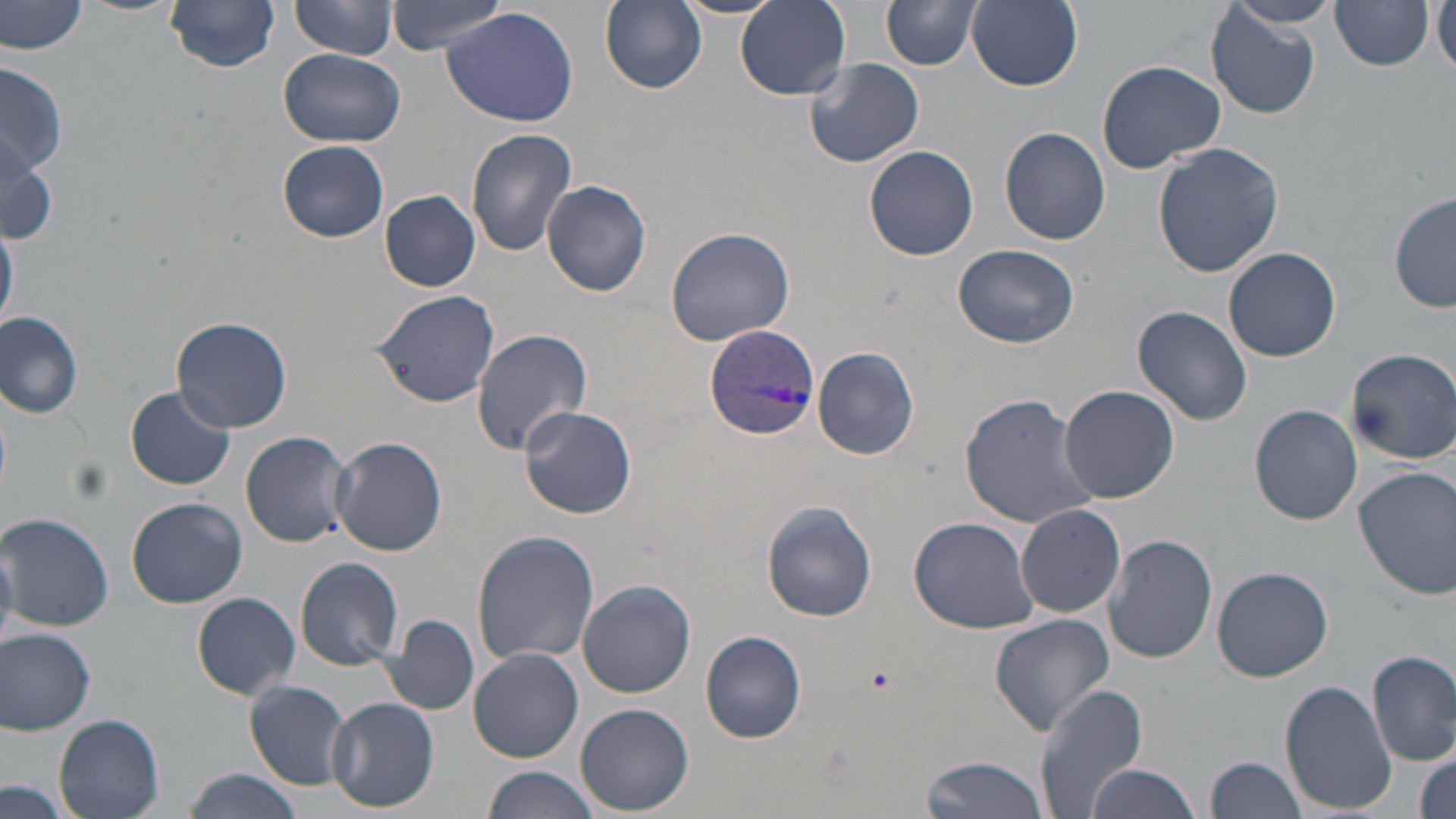
Summary:
  - Coordinate format: approximate bounding boxes as named x1/y1/x2/y2 corners in pixels
  - Plasmodium vivax-infected red blood cell locations: (x1=702, y1=322, x2=820, y2=442)
  - Platelet locations: (x1=861, y1=661, x2=896, y2=694)
  - Uninfected red blood cell locations: (x1=291, y1=0, x2=400, y2=58), (x1=386, y1=0, x2=517, y2=54), (x1=967, y1=0, x2=1083, y2=90), (x1=1, y1=1, x2=91, y2=56), (x1=165, y1=1, x2=281, y2=72), (x1=737, y1=1, x2=850, y2=98), (x1=885, y1=1, x2=981, y2=71), (x1=1230, y1=1, x2=1342, y2=27), (x1=1434, y1=1, x2=1455, y2=74), (x1=601, y1=3, x2=707, y2=93), (x1=1331, y1=3, x2=1434, y2=70), (x1=442, y1=7, x2=582, y2=128), (x1=1207, y1=8, x2=1318, y2=118), (x1=279, y1=48, x2=404, y2=147), (x1=805, y1=57, x2=925, y2=168), (x1=1097, y1=60, x2=1226, y2=173), (x1=1, y1=63, x2=66, y2=189), (x1=1, y1=126, x2=54, y2=244), (x1=465, y1=127, x2=577, y2=254), (x1=999, y1=127, x2=1112, y2=245), (x1=278, y1=140, x2=389, y2=242), (x1=1152, y1=142, x2=1283, y2=279), (x1=864, y1=145, x2=980, y2=260), (x1=541, y1=179, x2=653, y2=297), (x1=381, y1=190, x2=480, y2=291), (x1=1389, y1=193, x2=1455, y2=314), (x1=0, y1=212, x2=19, y2=332), (x1=664, y1=226, x2=798, y2=349), (x1=952, y1=243, x2=1080, y2=347), (x1=1224, y1=248, x2=1341, y2=362), (x1=371, y1=288, x2=501, y2=409), (x1=1131, y1=304, x2=1253, y2=426), (x1=0, y1=310, x2=86, y2=417), (x1=171, y1=316, x2=292, y2=432), (x1=471, y1=329, x2=592, y2=455), (x1=812, y1=347, x2=919, y2=460), (x1=1348, y1=347, x2=1456, y2=463), (x1=1057, y1=385, x2=1179, y2=503), (x1=126, y1=386, x2=234, y2=491), (x1=958, y1=392, x2=1099, y2=528), (x1=1250, y1=405, x2=1362, y2=524), (x1=520, y1=406, x2=636, y2=519), (x1=239, y1=430, x2=354, y2=547), (x1=332, y1=436, x2=446, y2=555), (x1=1355, y1=466, x2=1456, y2=600), (x1=125, y1=497, x2=247, y2=608), (x1=761, y1=500, x2=878, y2=621), (x1=1016, y1=503, x2=1126, y2=617), (x1=1, y1=511, x2=113, y2=632), (x1=909, y1=518, x2=1038, y2=634), (x1=472, y1=531, x2=599, y2=666), (x1=1104, y1=534, x2=1217, y2=664), (x1=0, y1=535, x2=17, y2=640), (x1=296, y1=557, x2=404, y2=669), (x1=1211, y1=566, x2=1333, y2=681), (x1=576, y1=578, x2=698, y2=697), (x1=192, y1=592, x2=300, y2=699), (x1=382, y1=614, x2=481, y2=715), (x1=988, y1=614, x2=1116, y2=737), (x1=0, y1=627, x2=97, y2=736), (x1=700, y1=630, x2=806, y2=743), (x1=469, y1=648, x2=584, y2=761), (x1=1366, y1=650, x2=1456, y2=767), (x1=244, y1=680, x2=352, y2=789), (x1=1034, y1=680, x2=1150, y2=818), (x1=1280, y1=681, x2=1394, y2=810), (x1=327, y1=697, x2=439, y2=812), (x1=577, y1=703, x2=693, y2=815), (x1=53, y1=714, x2=165, y2=818), (x1=1413, y1=745, x2=1456, y2=819), (x1=917, y1=754, x2=1050, y2=819), (x1=1207, y1=756, x2=1309, y2=819), (x1=1083, y1=762, x2=1199, y2=819), (x1=480, y1=764, x2=601, y2=819), (x1=184, y1=768, x2=297, y2=819), (x1=2, y1=780, x2=76, y2=818)
  - Slide-level diagnosis: Plasmodium vivax
  - Field of view: single
  - Image size: 1456×819 pixels
  - Modality: optical microscopy
  - Magnification: 1000x
  - Stain: May-Grünwald-Giemsa
  - Preparation: thin blood smear